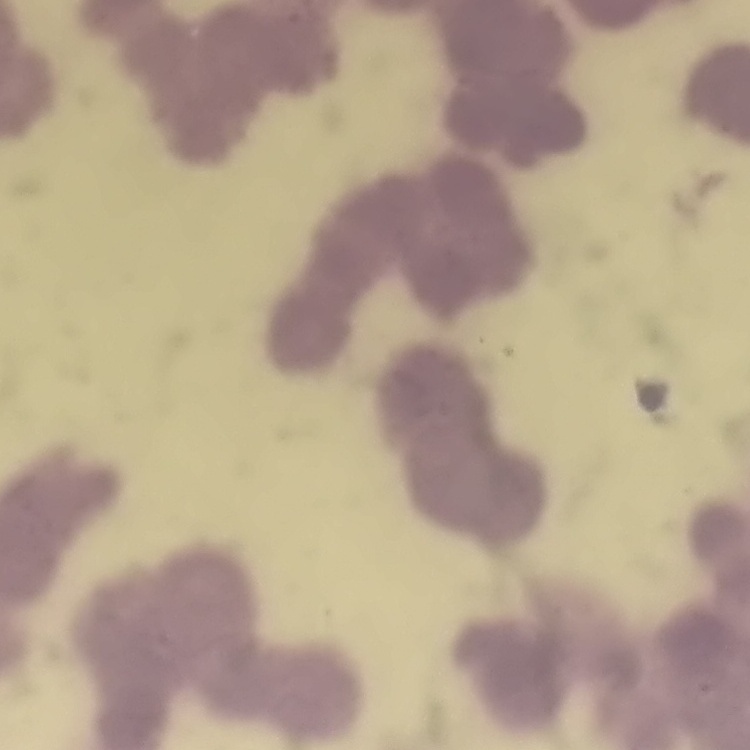
red blood cell morphology = rouleaux formation
stain = Field's or Giemsa
preparation = thin blood film
image type = square crop of a larger photomicrograph